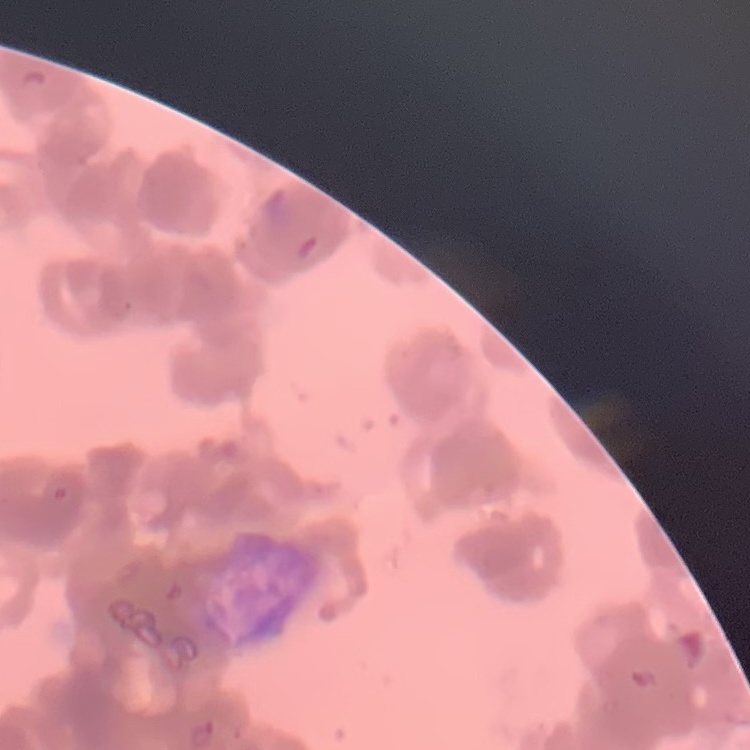 The red blood cells exhibit rouleaux formation. One tile cut from a larger photomicrograph. Thin blood smear. Stained with either Field's or Giemsa.